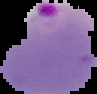
Summary:
  - Preparation: thin blood smear
  - Image type: segmented cell region on a black background
  - Result: Plasmodium parasites identified
  - Image size: 97×94 pixels